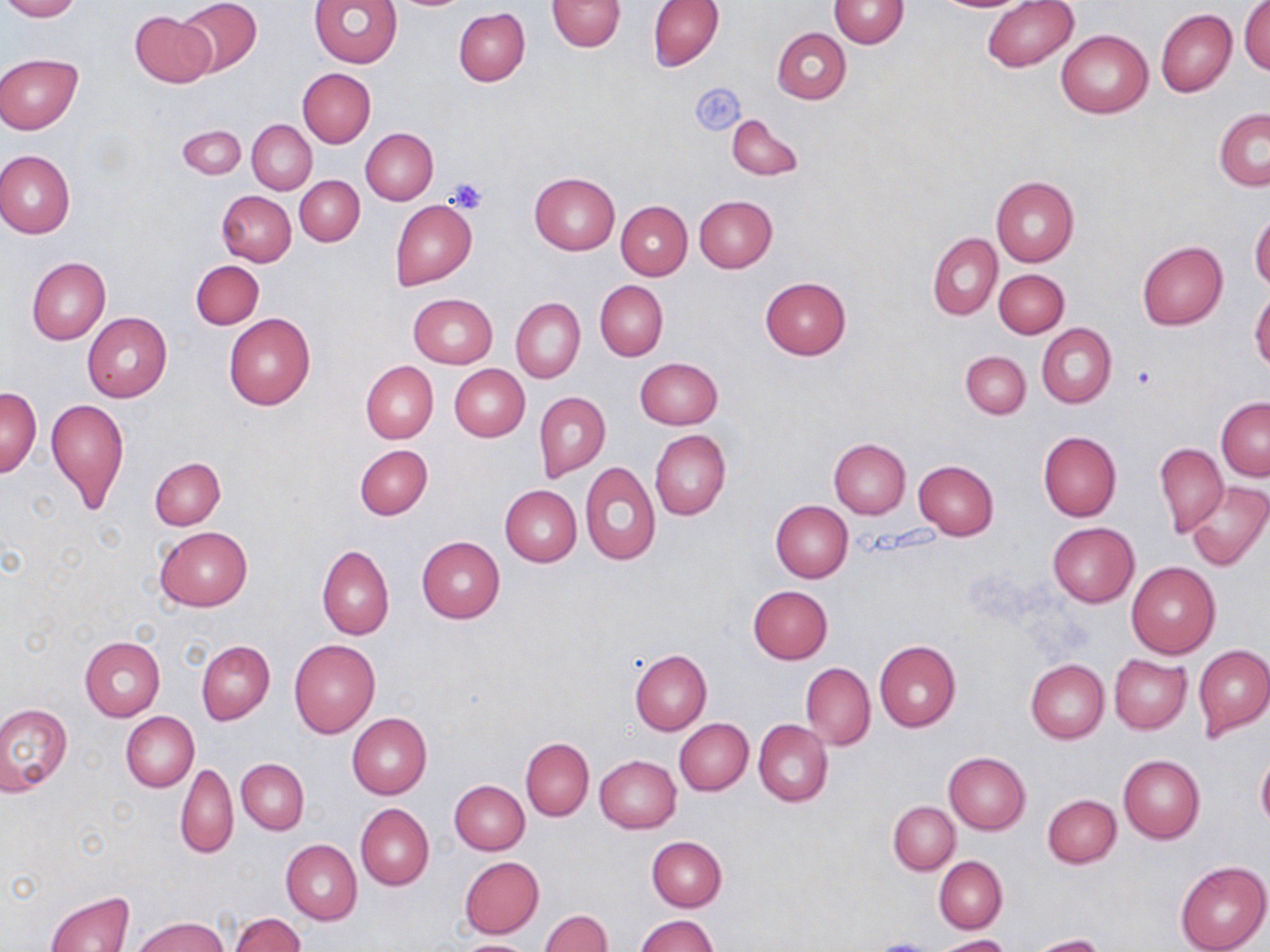
Approximate bounding boxes as named x1/y1/x2/y2 corners in pixels. Platelet locations: (x1=690, y1=81, x2=745, y2=135), (x1=444, y1=176, x2=491, y2=214), (x1=1131, y1=365, x2=1161, y2=393). Uninfected red blood cell locations: (x1=0, y1=0, x2=79, y2=21), (x1=175, y1=0, x2=263, y2=76), (x1=310, y1=0, x2=402, y2=68), (x1=547, y1=0, x2=626, y2=52), (x1=647, y1=0, x2=724, y2=70), (x1=932, y1=0, x2=1030, y2=12), (x1=983, y1=0, x2=1077, y2=72), (x1=829, y1=1, x2=908, y2=49), (x1=1239, y1=1, x2=1269, y2=74), (x1=454, y1=7, x2=530, y2=87), (x1=1155, y1=9, x2=1236, y2=97), (x1=130, y1=10, x2=217, y2=88), (x1=772, y1=27, x2=851, y2=103), (x1=1056, y1=29, x2=1153, y2=119), (x1=0, y1=54, x2=82, y2=133), (x1=298, y1=68, x2=376, y2=147), (x1=1213, y1=109, x2=1270, y2=191), (x1=726, y1=112, x2=803, y2=182), (x1=248, y1=120, x2=316, y2=193), (x1=177, y1=125, x2=246, y2=179), (x1=361, y1=128, x2=438, y2=204), (x1=0, y1=150, x2=75, y2=237), (x1=529, y1=173, x2=619, y2=254), (x1=295, y1=176, x2=364, y2=245), (x1=991, y1=176, x2=1079, y2=266), (x1=217, y1=190, x2=296, y2=267), (x1=694, y1=195, x2=777, y2=272), (x1=391, y1=200, x2=477, y2=290), (x1=617, y1=201, x2=692, y2=280), (x1=1250, y1=211, x2=1270, y2=291), (x1=928, y1=232, x2=1002, y2=319), (x1=1137, y1=241, x2=1228, y2=329), (x1=26, y1=257, x2=111, y2=344), (x1=191, y1=260, x2=263, y2=329), (x1=994, y1=269, x2=1069, y2=338), (x1=760, y1=276, x2=852, y2=359), (x1=595, y1=280, x2=667, y2=361), (x1=1250, y1=288, x2=1270, y2=372), (x1=409, y1=294, x2=497, y2=367), (x1=511, y1=297, x2=585, y2=382), (x1=224, y1=312, x2=316, y2=409), (x1=83, y1=313, x2=172, y2=402), (x1=1036, y1=323, x2=1116, y2=409), (x1=961, y1=351, x2=1030, y2=419), (x1=635, y1=357, x2=723, y2=429), (x1=361, y1=361, x2=438, y2=443), (x1=449, y1=364, x2=529, y2=441), (x1=1, y1=387, x2=41, y2=478), (x1=535, y1=391, x2=610, y2=482), (x1=46, y1=397, x2=129, y2=514), (x1=1216, y1=398, x2=1270, y2=480), (x1=650, y1=429, x2=731, y2=520), (x1=1037, y1=432, x2=1123, y2=520), (x1=829, y1=438, x2=910, y2=518), (x1=1155, y1=443, x2=1227, y2=537), (x1=354, y1=444, x2=433, y2=520), (x1=150, y1=459, x2=224, y2=530), (x1=914, y1=461, x2=999, y2=539), (x1=580, y1=462, x2=660, y2=565), (x1=1186, y1=481, x2=1268, y2=570), (x1=501, y1=485, x2=581, y2=566), (x1=771, y1=500, x2=853, y2=581), (x1=1047, y1=523, x2=1139, y2=608), (x1=154, y1=527, x2=252, y2=611), (x1=416, y1=536, x2=506, y2=623), (x1=317, y1=545, x2=393, y2=639), (x1=1126, y1=561, x2=1220, y2=658), (x1=748, y1=585, x2=833, y2=664), (x1=79, y1=636, x2=165, y2=720), (x1=290, y1=639, x2=381, y2=738), (x1=196, y1=640, x2=275, y2=724), (x1=875, y1=640, x2=961, y2=732), (x1=1194, y1=645, x2=1270, y2=739), (x1=629, y1=650, x2=711, y2=735), (x1=1109, y1=655, x2=1191, y2=733), (x1=1026, y1=659, x2=1109, y2=742), (x1=801, y1=662, x2=875, y2=750), (x1=0, y1=704, x2=72, y2=794), (x1=121, y1=712, x2=198, y2=791), (x1=347, y1=713, x2=432, y2=799), (x1=675, y1=719, x2=753, y2=796), (x1=753, y1=720, x2=832, y2=807), (x1=521, y1=737, x2=593, y2=821), (x1=944, y1=751, x2=1030, y2=834), (x1=1257, y1=753, x2=1270, y2=831), (x1=1119, y1=754, x2=1206, y2=844), (x1=595, y1=755, x2=680, y2=834), (x1=237, y1=758, x2=310, y2=833), (x1=175, y1=764, x2=238, y2=859), (x1=449, y1=780, x2=529, y2=855), (x1=1042, y1=794, x2=1121, y2=868), (x1=889, y1=801, x2=960, y2=873), (x1=355, y1=803, x2=433, y2=889), (x1=647, y1=837, x2=727, y2=911), (x1=281, y1=840, x2=362, y2=924), (x1=933, y1=856, x2=1007, y2=933), (x1=459, y1=857, x2=544, y2=937), (x1=1175, y1=860, x2=1270, y2=952), (x1=44, y1=891, x2=135, y2=952), (x1=539, y1=910, x2=611, y2=952), (x1=229, y1=912, x2=306, y2=952), (x1=636, y1=914, x2=718, y2=952), (x1=135, y1=917, x2=229, y2=952), (x1=937, y1=934, x2=1012, y2=952), (x1=1032, y1=934, x2=1106, y2=952), (x1=453, y1=938, x2=539, y2=952). Slide-level diagnosis: negative for blood parasites. May-Grünwald-Giemsa stain. Single field of view. Thin blood film. Light microscopy. Image is 1270×952 pixels. 1000x magnification.